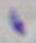
magnification = 1000x
modality = photomicrograph
identification = Toxoplasma gondii